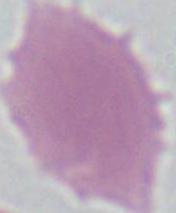
A red blood cell is shown. 1000x magnification. Photomicrograph.